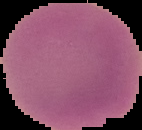
Summary:
  - Preparation: thin blood film
  - Malaria status: uninfected
  - Image type: cell region segmented out of the field of view; surrounding area masked to black
  - Image size: 142×130 pixels